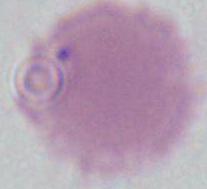
modality = photomicrograph
magnification = 1000x
identification = red blood cell